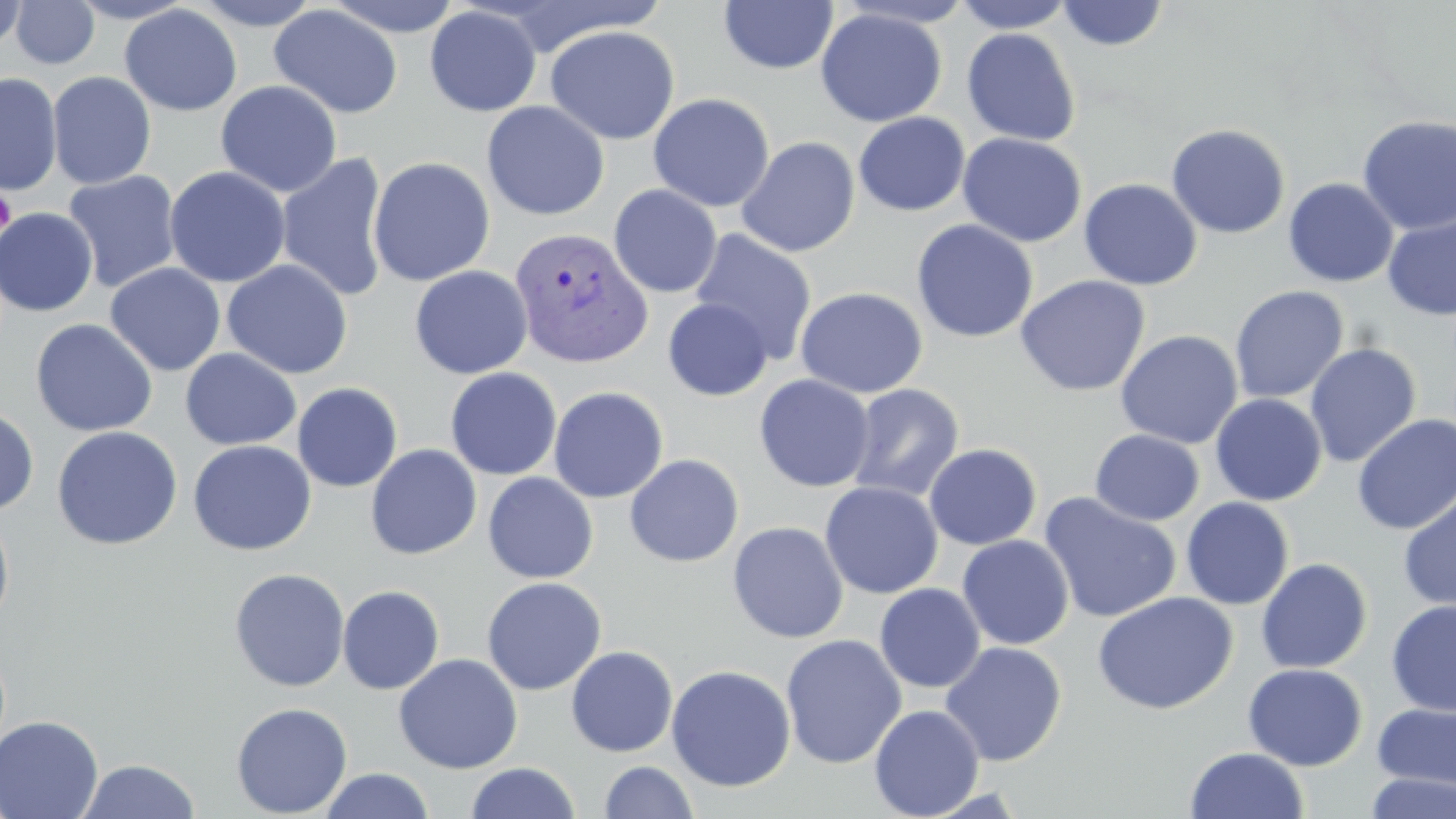

slide-level diagnosis = Plasmodium vivax
stain = May-Grünwald-Giemsa
magnification = 1000x
Plasmodium vivax-infected red blood cell locations = approximate bounding boxes as [x1, y1, x2, y2] in pixels: [509, 226, 653, 370]
uninfected red blood cell locations = approximate bounding boxes as [x1, y1, x2, y2] in pixels: [0, 0, 28, 55], [65, 0, 197, 24], [190, 0, 324, 30], [324, 0, 464, 37], [952, 0, 1077, 33], [9, 1, 100, 69], [719, 1, 838, 74], [1056, 1, 1170, 51], [120, 4, 243, 117], [269, 4, 403, 119], [425, 6, 541, 116], [815, 8, 947, 127], [422, 17, 670, 124], [544, 25, 681, 144], [961, 28, 1081, 146], [47, 71, 156, 189], [0, 73, 62, 196], [215, 80, 342, 197], [648, 93, 774, 212], [481, 101, 609, 220], [853, 112, 970, 216], [1357, 115, 1456, 235], [1165, 123, 1291, 238], [957, 132, 1087, 248], [736, 136, 860, 258], [275, 152, 391, 304], [367, 156, 495, 286], [165, 166, 291, 288], [62, 170, 183, 293], [1283, 177, 1399, 287], [1078, 178, 1203, 290], [608, 185, 722, 298], [0, 207, 98, 317], [1382, 214, 1456, 321], [912, 219, 1038, 343], [689, 229, 817, 366], [222, 259, 353, 378], [105, 263, 226, 376], [410, 265, 533, 379], [1015, 275, 1150, 397], [1229, 285, 1349, 403], [794, 287, 928, 398], [662, 297, 773, 401], [30, 318, 157, 437], [1114, 330, 1243, 449], [1304, 342, 1422, 468], [180, 348, 301, 450], [445, 367, 562, 480], [754, 374, 876, 492], [292, 382, 403, 492], [846, 383, 965, 503], [548, 386, 668, 503], [1210, 394, 1328, 506], [0, 406, 39, 515], [1351, 414, 1456, 535], [51, 426, 183, 550], [1090, 429, 1204, 526], [187, 440, 317, 556], [923, 443, 1042, 550], [365, 444, 482, 560], [624, 454, 744, 567], [482, 472, 599, 583], [819, 481, 943, 599], [1397, 489, 1456, 613], [1038, 492, 1182, 624], [1181, 497, 1294, 610], [0, 508, 16, 632], [727, 521, 849, 644], [956, 535, 1074, 650], [1256, 558, 1373, 674], [228, 568, 350, 692], [481, 577, 607, 695], [874, 583, 986, 693], [337, 585, 444, 695], [1091, 591, 1238, 715], [1386, 600, 1456, 717], [780, 634, 907, 769], [939, 642, 1066, 766], [566, 645, 678, 757], [393, 653, 522, 773], [1242, 663, 1368, 770], [666, 664, 796, 792], [231, 701, 353, 818], [1371, 702, 1456, 791], [869, 704, 984, 819], [0, 715, 104, 819], [1184, 747, 1309, 819], [75, 758, 201, 818], [599, 760, 699, 819], [465, 762, 581, 819], [318, 768, 436, 819], [1363, 771, 1456, 819]
preparation = thin blood smear
image size = 1456×819 pixels
platelet locations = approximate bounding boxes as [x1, y1, x2, y2] in pixels: [1, 187, 16, 239]
modality = light microscopy
field of view = single